Outline each Plasmodium falciparum-infected red blood cell.
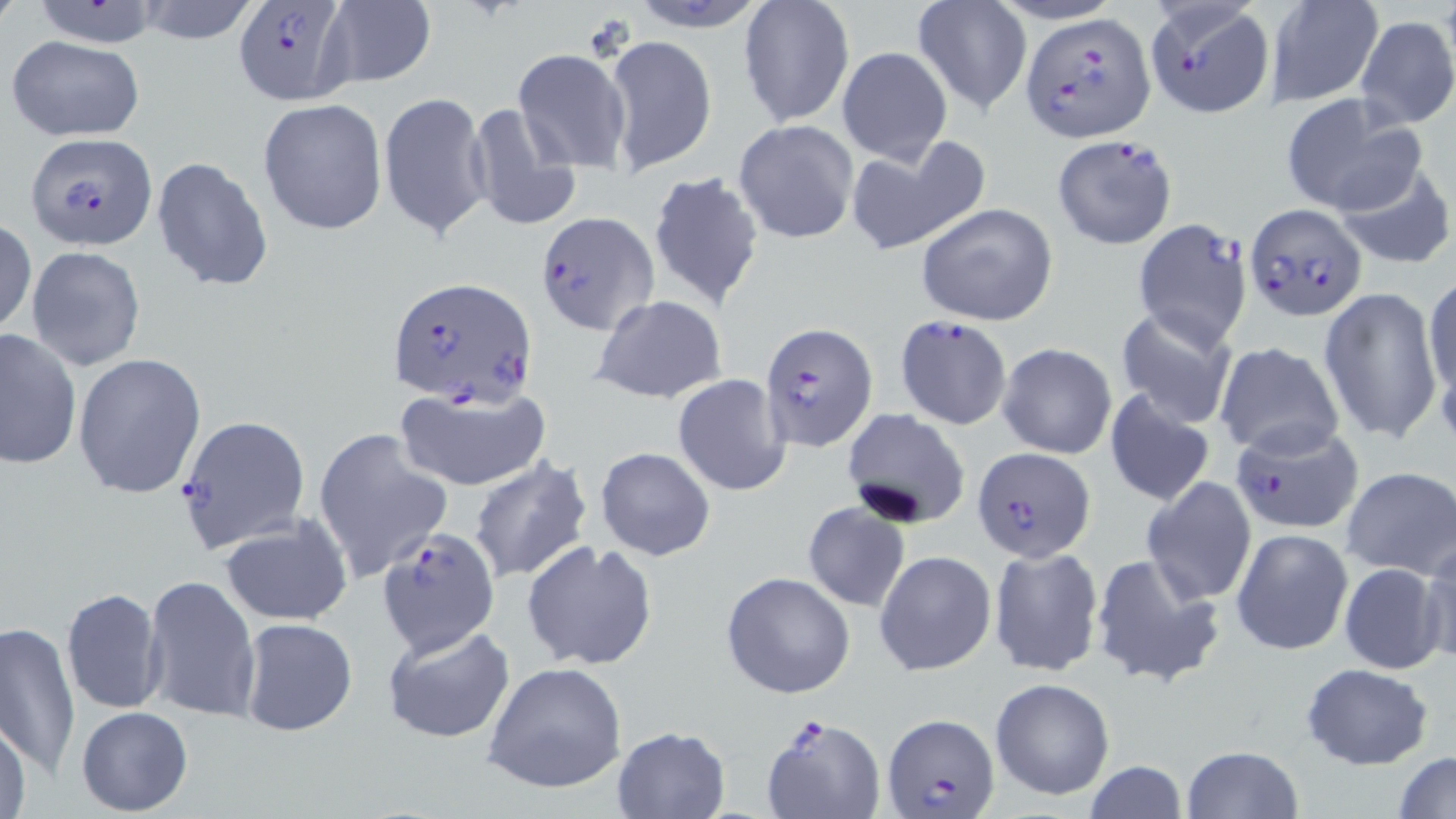
Approximate bounding boxes as (x1, y1, x2, y2) in pixels.
Plasmodium falciparum-infected red blood cells: (232, 0, 353, 105), (1144, 0, 1274, 120), (1021, 13, 1154, 140), (25, 132, 158, 249), (1052, 135, 1177, 250), (1243, 203, 1366, 321), (533, 210, 656, 336), (1131, 219, 1253, 352), (387, 275, 538, 406), (895, 314, 1013, 430), (759, 322, 878, 451), (176, 414, 312, 554), (1227, 419, 1358, 533), (971, 446, 1094, 564), (377, 527, 499, 654), (760, 714, 886, 819), (883, 714, 998, 818).

Platelet locations: (582, 13, 635, 63). Uninfected red blood cell locations: (0, 0, 22, 32), (132, 0, 263, 45), (621, 0, 775, 32), (25, 1, 167, 50), (738, 1, 855, 128), (912, 1, 1032, 116), (1263, 1, 1385, 107), (318, 2, 438, 89), (1355, 13, 1455, 129), (605, 33, 717, 172), (6, 35, 146, 142), (837, 46, 952, 165), (512, 48, 633, 169), (378, 90, 491, 240), (1281, 94, 1425, 217), (257, 98, 388, 236), (464, 103, 582, 233), (733, 118, 860, 245), (844, 134, 990, 256), (151, 155, 272, 291), (1329, 155, 1455, 269), (646, 170, 766, 309), (914, 202, 1060, 325), (1, 218, 37, 339), (24, 245, 146, 372), (1422, 274, 1456, 411), (1320, 285, 1443, 446), (591, 295, 728, 404), (1115, 307, 1238, 429), (0, 327, 81, 471), (1213, 341, 1343, 459), (998, 343, 1116, 459), (74, 352, 206, 498), (673, 373, 793, 497), (395, 385, 553, 491), (1103, 387, 1218, 508), (842, 409, 972, 530), (313, 429, 453, 584), (596, 447, 716, 561), (468, 455, 593, 585), (1341, 467, 1456, 578), (1141, 475, 1257, 607), (801, 501, 910, 611), (218, 515, 352, 627), (1231, 527, 1354, 655), (1418, 537, 1456, 667), (522, 540, 659, 672), (988, 545, 1106, 679), (875, 551, 996, 675), (1091, 552, 1227, 690), (1337, 562, 1448, 675), (721, 571, 855, 699), (142, 575, 261, 724), (61, 586, 167, 717), (238, 617, 359, 738), (0, 618, 80, 784), (381, 623, 517, 745), (483, 661, 628, 793), (1300, 662, 1436, 769), (990, 677, 1115, 800), (76, 706, 193, 816), (0, 719, 31, 819), (612, 726, 730, 818), (1179, 745, 1306, 819), (1393, 749, 1456, 819), (1082, 761, 1190, 818). Slide-level diagnosis: Plasmodium falciparum. Image is 1456×819 pixels. Single field of view. May-Grünwald-Giemsa-stained preparation. Thin blood smear. Optical microscopy. 1000x magnification.